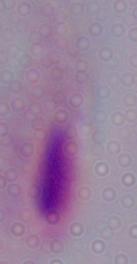

Summary:
  - Identification: trichomonad
  - Modality: photomicrograph
  - Magnification: 1000x